Assess this cell for malaria.
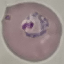

It is parasitized.

{
  "capture": "smartphone camera at the microscope eyepiece",
  "stain": "Giemsa",
  "image_type": "automatically extracted cell patch, resized to 64 × 64 pixels",
  "preparation": "thin blood smear"
}